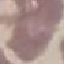

Malaria status: uninfected. Cell patch, automatically extracted from a larger field of view and resized to 64 × 64 pixels. Giemsa-stained preparation. Photographed with a smartphone camera at the microscope eyepiece. Thin smear of blood.